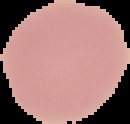

Summary:
  - Image type: segmented cell region with the area outside set to black
  - Preparation: thin blood film
  - Malaria status: uninfected
  - Image size: 130×124 pixels